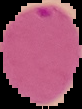 From a thin blood film. The area outside the segmented cell region is set to black. Malaria status: parasitized. Image is 82×109 pixels.